Classify this cell by malaria status.
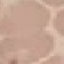

It is uninfected.

stain = Giemsa
capture = smartphone through the microscope eyepiece
image type = automatically extracted cell patch, resized to 64 × 64 pixels
preparation = thin blood smear